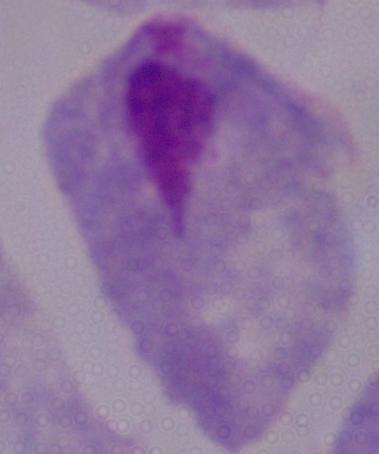 A trichomonad is shown. Photomicrograph. 1000x magnification.